Assess this cell for malaria.
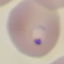

It is parasitized.

stain = Giemsa
capture = smartphone camera at the microscope eyepiece
preparation = thin blood smear
image type = cell patch, automatically extracted from a larger field of view and resized to 64 × 64 pixels